Describe the morphology of the erythrocytes.
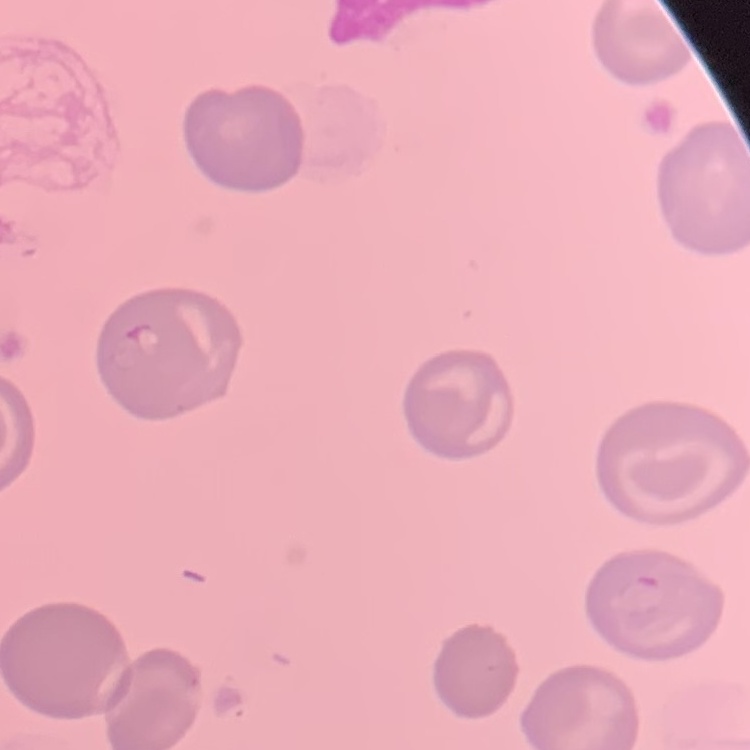

They show no rouleaux formation.

Thin blood smear. Field's or Giemsa stain. Square crop of a larger photomicrograph.